Identify the parasite.
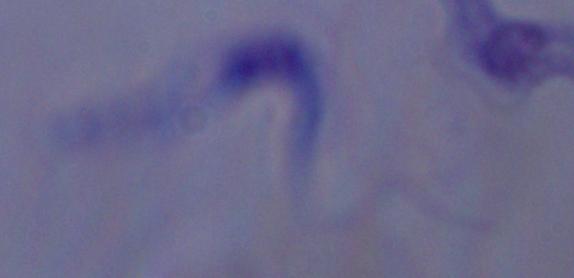

A trypanosome.

Captured at 1000x magnification. Photomicrograph.